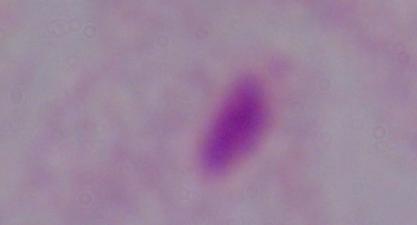
Summary:
  - Modality: photomicrograph
  - Identification: trichomonad
  - Magnification: 1000x